Assess this cell for malaria.
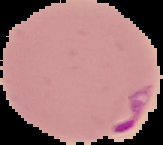
It is parasitized.

Summary:
  - Image size: 163×145 pixels
  - Image type: segmented cell region on a black background
  - Preparation: thin blood smear